Locate and identify every blood parasite.
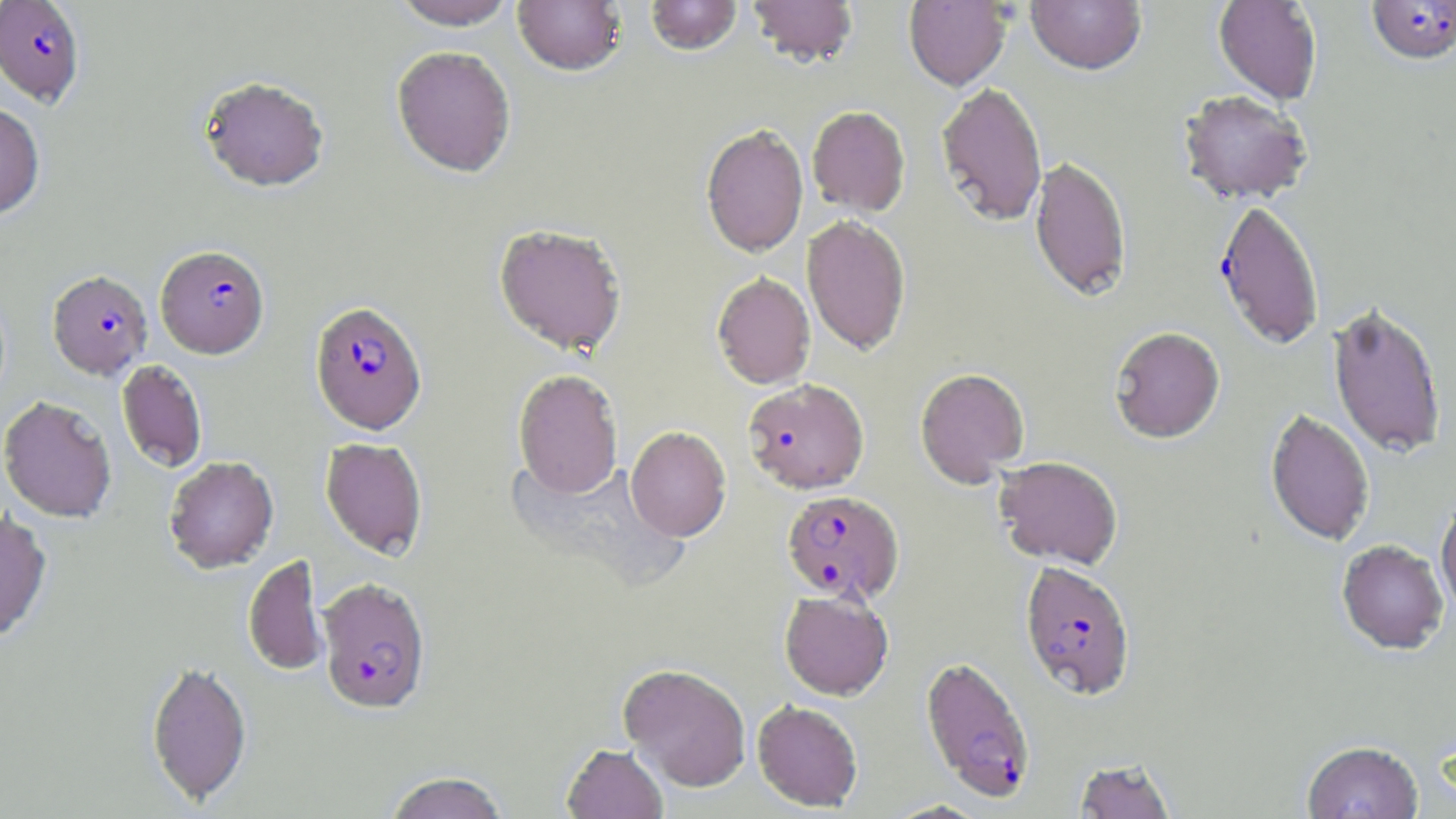
Approximate bounding boxes as (x1, y1, x2, y2) in pixels.
Plasmodium falciparum-infected red blood cells: (0, 0, 85, 106), (1365, 1, 1456, 67), (1212, 199, 1325, 352), (155, 245, 270, 359), (47, 270, 153, 380), (310, 301, 428, 435), (742, 380, 870, 496), (781, 490, 905, 606), (1019, 562, 1136, 701), (317, 578, 432, 716), (920, 656, 1036, 803).
No Plasmodium ovale, Plasmodium malariae, Plasmodium vivax, Babesia divergens, or Trypanosoma brucei observed.

slide_level_diagnosis: Plasmodium falciparum
stain: May-Grünwald-Giemsa
magnification: 1000x
image_size: 1456×819 pixels
preparation: thin blood film
uninfected_red_blood_cell_locations: 'approximate bounding boxes as (x1, y1, x2, y2) in pixels: (391, 0, 518, 30), (646, 0, 742, 57), (747, 0, 859, 69), (903, 0, 1012, 91), (1026, 0, 1146, 77), (1212, 0, 1322, 106), (513, 1, 626, 77), (391, 46, 516, 178), (198, 76, 330, 193), (936, 82, 1047, 228), (1177, 91, 1312, 206), (0, 102, 45, 220), (807, 106, 911, 218), (700, 124, 808, 259), (1029, 156, 1131, 303), (802, 216, 911, 356), (492, 224, 628, 358), (711, 272, 815, 390), (1328, 303, 1447, 461), (1109, 327, 1225, 445), (116, 360, 207, 474), (915, 368, 1030, 488), (513, 369, 623, 500), (1, 395, 117, 524), (1265, 409, 1375, 548), (625, 426, 731, 542), (320, 438, 427, 560), (164, 456, 279, 574), (994, 457, 1123, 570), (1436, 500, 1456, 617), (0, 507, 53, 644), (1336, 542, 1448, 657), (242, 554, 328, 677), (779, 591, 893, 702), (145, 660, 253, 807), (618, 664, 751, 792), (752, 701, 863, 812), (1302, 742, 1423, 819), (562, 744, 668, 819), (1073, 759, 1177, 819), (384, 771, 509, 819), (883, 800, 989, 818)'
modality: optical microscopy
field_of_view: single